Name the parasite shown.
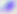

This is Toxoplasma gondii.

Summary:
  - Magnification: 400x
  - Modality: micrograph